Classify this cell by malaria status.
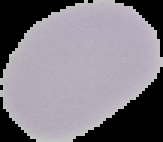

Uninfected.

Cell region segmented out of the field of view; the surrounding area is masked to black. From a thin blood smear. Image is 163×142 pixels.